Describe the morphology of the red blood cells.
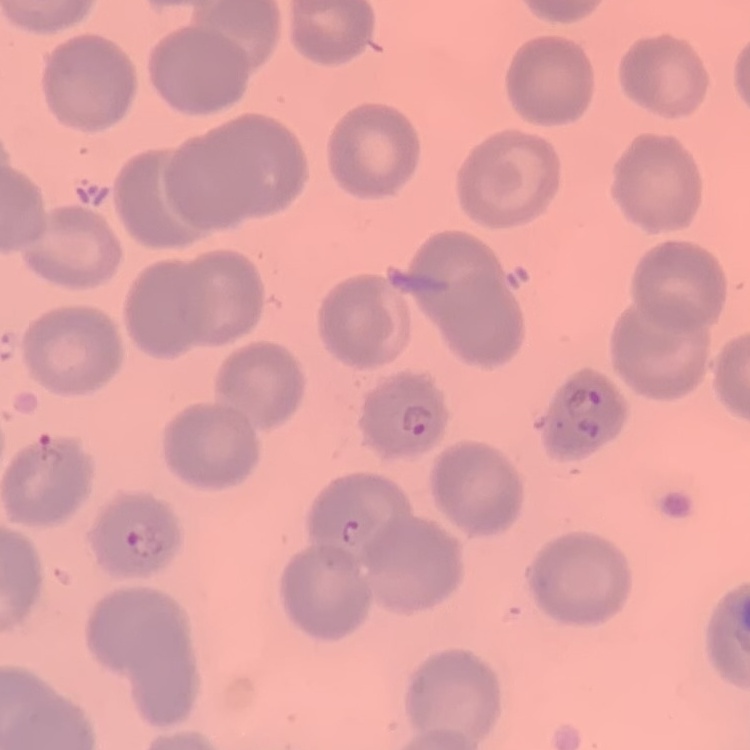
No rouleaux formation.

Summary:
  - Preparation: thin peripheral smear
  - Stain: Field's or Giemsa
  - Image type: square crop of a larger photomicrograph